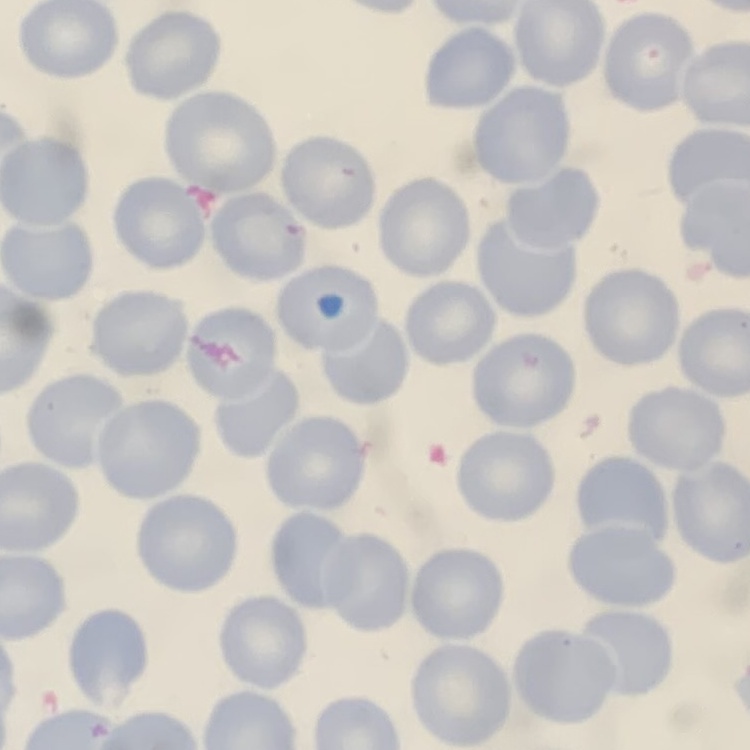

The erythrocytes exhibit no rouleaux formation. Thin peripheral smear. Stained with either Field's or Giemsa. Square crop of a larger photomicrograph.